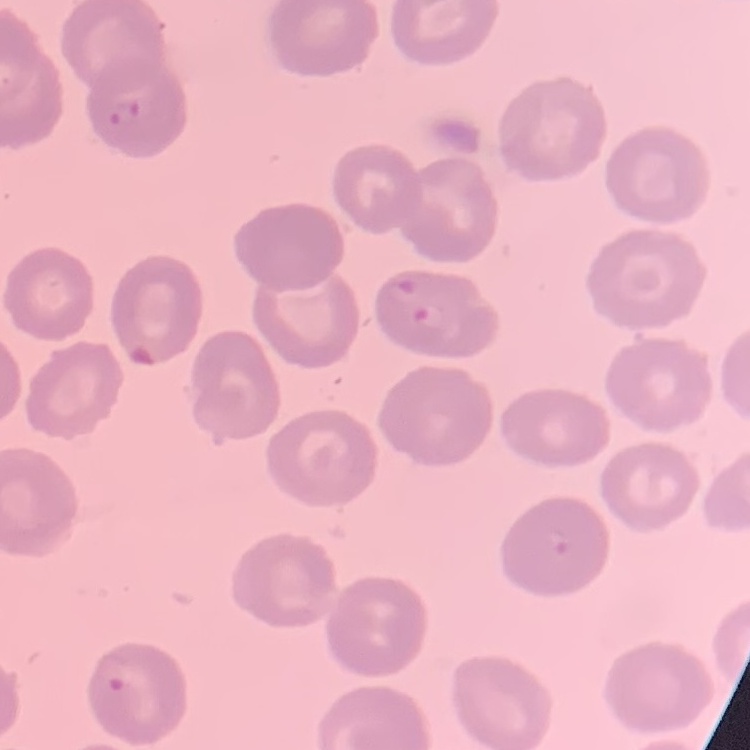
Summary:
  - Erythrocyte morphology: no rouleaux formation
  - Stain: Field's or Giemsa
  - Image type: one tile cut from a larger photomicrograph
  - Preparation: thin blood film